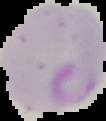
preparation = thin blood smear
image size = 106×121 pixels
result = malaria parasites detected
image type = cell region segmented out of the field of view; surrounding area masked to black